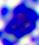

{
  "modality": "photomicrograph",
  "identification": "white blood cell",
  "magnification": "400x"
}